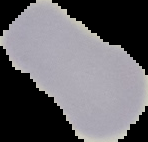 Result: negative for Plasmodium parasites. From a thin blood smear. The area outside the segmented cell region is set to black. Image is 148×142 pixels.